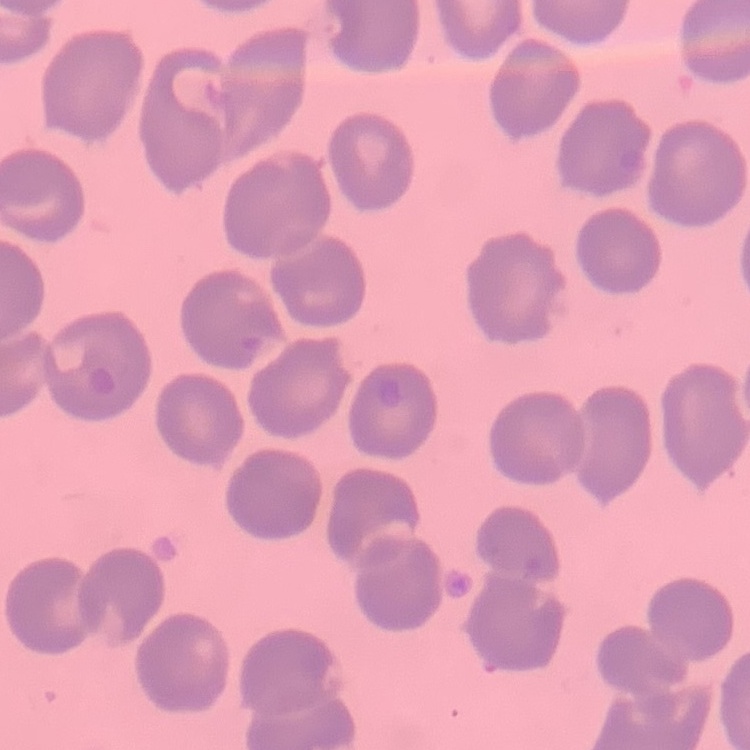
Summary:
  - Red blood cell morphology: no rouleaux formation
  - Preparation: thin peripheral smear
  - Image type: square crop of a larger photomicrograph
  - Stain: Field's or Giemsa